Assess this cell for malaria.
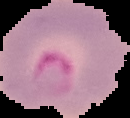
Parasitized.

image size = 130×118 pixels
image type = segmented cell region on a black background
preparation = thin blood film